Assess this cell for malaria.
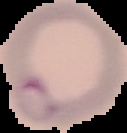

Parasitized.

image size = 127×133 pixels
preparation = thin blood smear
image type = segmented cell region with the area outside set to black